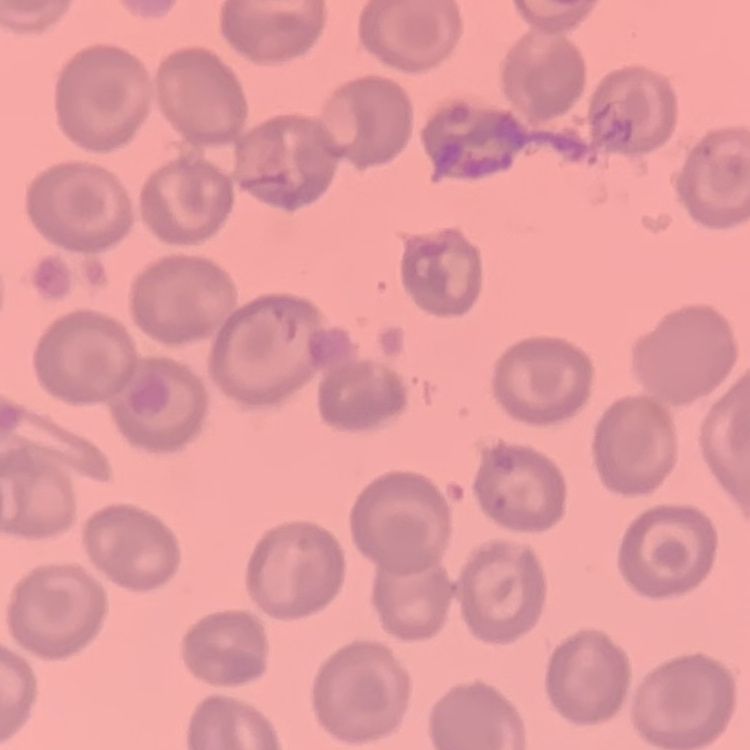
Summary:
  - Erythrocyte morphology: no rouleaux formation
  - Preparation: thin blood film
  - Image type: one tile cut from a larger photomicrograph
  - Stain: Field's or Giemsa